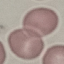
result = no malaria parasites detected
image type = cell patch, automatically extracted from a larger field of view and resized to 64 × 64 pixels
stain = Giemsa
capture = smartphone through the microscope eyepiece
preparation = thin smear